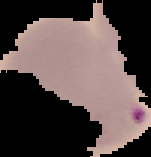
Summary:
  - Malaria status: parasitized
  - Image type: cell region segmented out of the field of view; surrounding area masked to black
  - Image size: 151×157 pixels
  - Preparation: thin blood film